Classify this cell by malaria status.
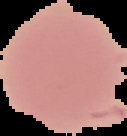

It is uninfected.

Summary:
  - Image size: 127×136 pixels
  - Preparation: thin blood smear
  - Image type: segmented cell region on a black background